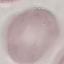

malaria status = uninfected
capture = smartphone through the microscope eyepiece
stain = Giemsa
preparation = thin smear
image type = cell patch, automatically extracted from a larger field of view and resized to 64 × 64 pixels